Give the position of every Plasmodium parasite.
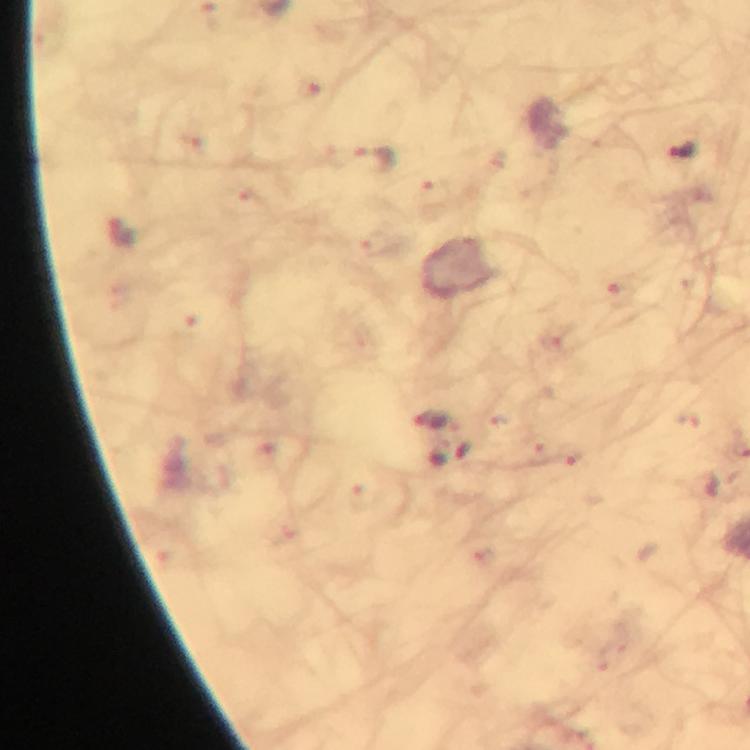

Approximate centers as (x, y) in pixels.
Plasmodium parasites: (682, 149), (375, 161), (430, 422), (448, 452).

Thick blood smear. Immersion oil was used. From a malaria diagnostic workup. Photographed with a smartphone mounted on the microscope. Giemsa stain. Image is 750×750 pixels. At 100x magnification. A crop from one field of view.